Give a bounding box for every parasitised red blood cell.
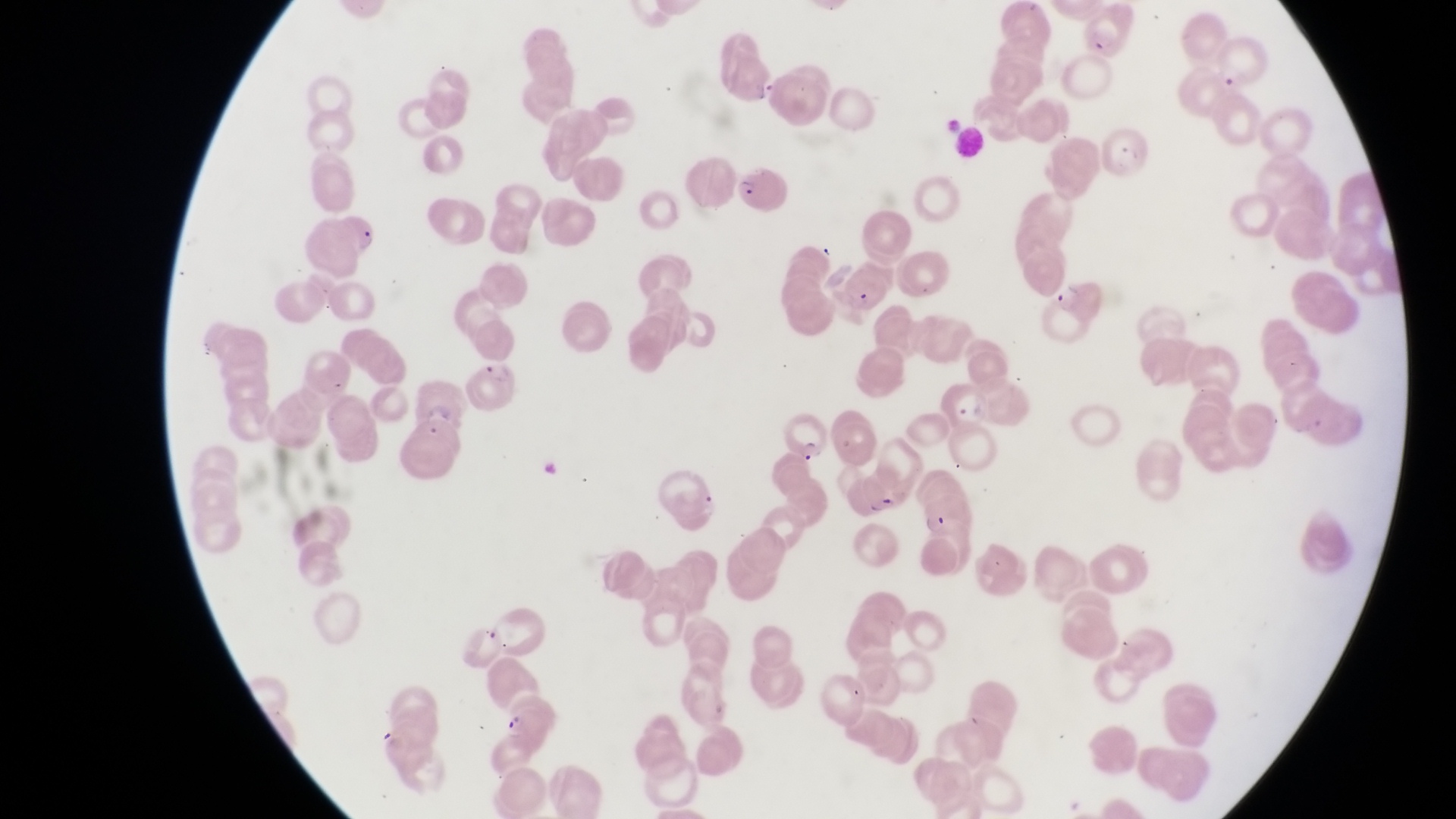
Approximate bounding boxes as left top right bottom in pixels.
Parasitised red blood cells: 1103 122 1157 183; 735 159 791 212; 1047 272 1106 330; 938 377 991 427; 786 407 839 465.

Summary:
  - Trophozoite locations: 920 510 952 541
  - Artifact (platelet-like body, stain precipitate, or debris) locations: 750 74 782 108
  - Preparation: thin blood smear
  - Image size: 1456×819 pixels
  - Field of view: single
  - Magnification: 1000x
  - Country: Uganda
  - Capture: smartphone photograph through the eyepiece of an Olympus CX-23 microscope